Classify this cell by malaria status.
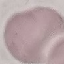

Uninfected.

preparation = thin smear
image type = cell patch, automatically extracted from a larger field of view and resized to 64 × 64 pixels
stain = Giemsa
capture = smartphone through the microscope eyepiece